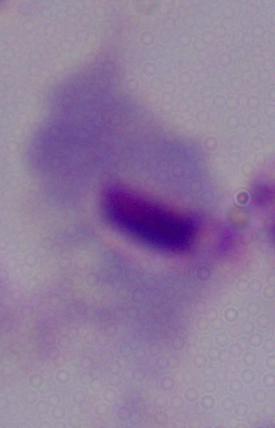 A trichomonad is shown. Micrograph. Captured at 1000x magnification.